Outline each blood parasite and name the species.
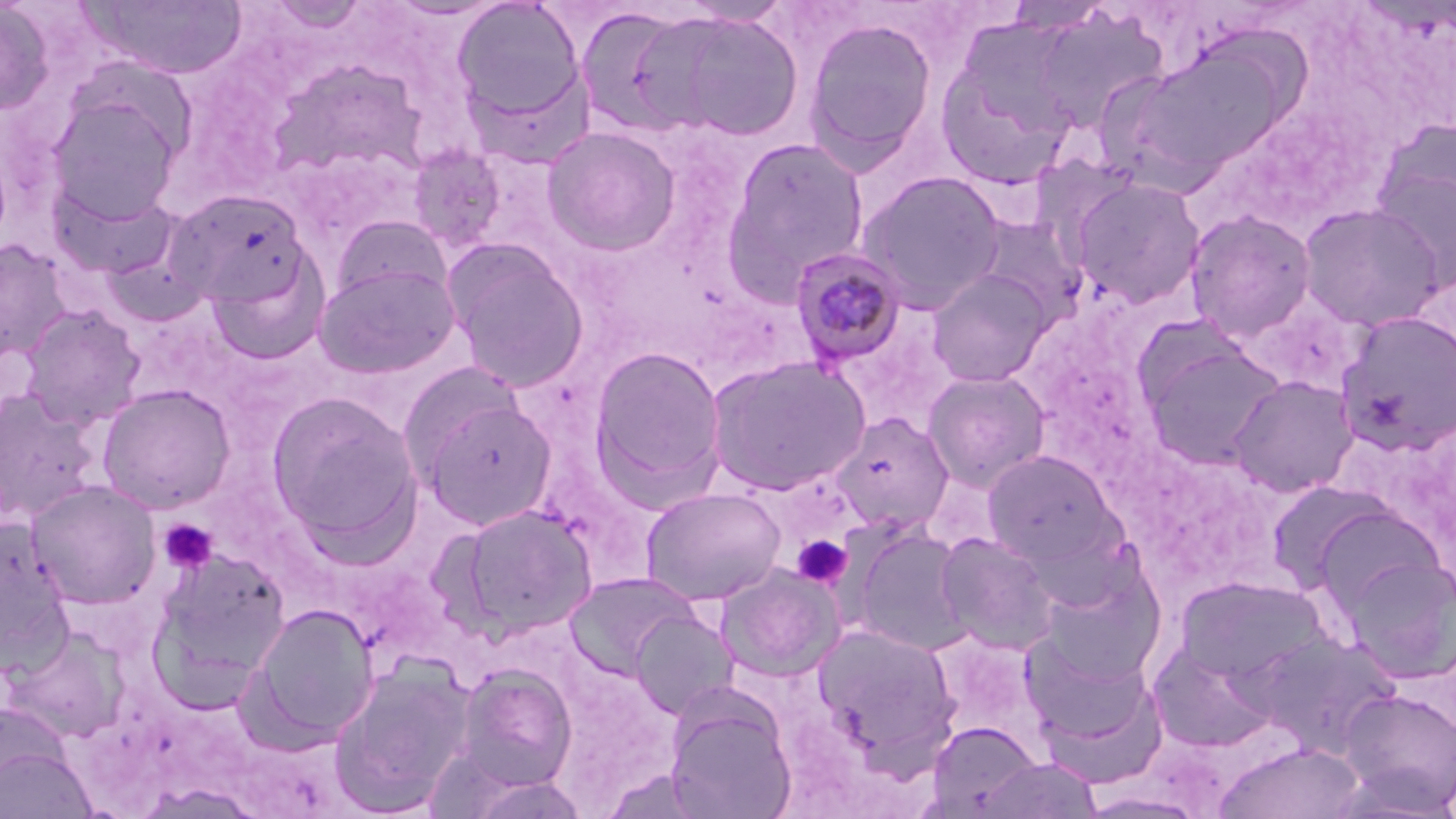

Approximate bounding boxes as named x1/y1/x2/y2 corners in pixels.
Plasmodium malariae-infected red blood cells: (x1=789, y1=247, x2=908, y2=368).
No Plasmodium falciparum, Plasmodium ovale, Plasmodium vivax, Babesia divergens, or Trypanosoma brucei observed.

slide-level diagnosis = Plasmodium malariae
modality = light microscopy
preparation = thin blood smear
magnification = 1000x
platelet locations = approximate bounding boxes as named x1/y1/x2/y2 corners in pixels: (x1=159, y1=519, x2=218, y2=574), (x1=791, y1=535, x2=852, y2=588)
uninfected red blood cell locations = approximate bounding boxes as named x1/y1/x2/y2 corners in pixels: (x1=450, y1=0, x2=588, y2=138), (x1=0, y1=1, x2=54, y2=116), (x1=79, y1=1, x2=250, y2=80), (x1=665, y1=11, x2=806, y2=141), (x1=801, y1=15, x2=939, y2=169), (x1=934, y1=36, x2=1082, y2=192), (x1=1123, y1=40, x2=1296, y2=184), (x1=47, y1=90, x2=185, y2=224), (x1=541, y1=125, x2=682, y2=256), (x1=722, y1=136, x2=871, y2=296), (x1=406, y1=143, x2=508, y2=255), (x1=1370, y1=153, x2=1456, y2=297), (x1=855, y1=170, x2=1008, y2=313), (x1=1070, y1=176, x2=1207, y2=308), (x1=49, y1=177, x2=183, y2=282), (x1=168, y1=188, x2=312, y2=310), (x1=1297, y1=202, x2=1446, y2=332), (x1=1184, y1=209, x2=1317, y2=342), (x1=330, y1=214, x2=453, y2=307), (x1=969, y1=214, x2=1088, y2=325), (x1=0, y1=239, x2=74, y2=363), (x1=442, y1=239, x2=591, y2=393), (x1=205, y1=247, x2=332, y2=364), (x1=314, y1=261, x2=461, y2=379), (x1=927, y1=269, x2=1053, y2=386), (x1=18, y1=305, x2=146, y2=429), (x1=1336, y1=310, x2=1456, y2=455), (x1=1140, y1=337, x2=1286, y2=469), (x1=588, y1=346, x2=729, y2=505), (x1=705, y1=354, x2=871, y2=496), (x1=921, y1=369, x2=1051, y2=492), (x1=1228, y1=375, x2=1358, y2=498), (x1=97, y1=383, x2=237, y2=514), (x1=0, y1=387, x2=102, y2=524), (x1=267, y1=391, x2=422, y2=548), (x1=416, y1=392, x2=559, y2=531), (x1=831, y1=413, x2=954, y2=534), (x1=981, y1=450, x2=1122, y2=571), (x1=26, y1=479, x2=162, y2=609), (x1=1265, y1=482, x2=1397, y2=596), (x1=641, y1=486, x2=786, y2=606), (x1=458, y1=503, x2=598, y2=636), (x1=1308, y1=503, x2=1446, y2=618), (x1=0, y1=520, x2=74, y2=669), (x1=852, y1=528, x2=974, y2=656), (x1=936, y1=532, x2=1061, y2=655), (x1=151, y1=547, x2=291, y2=698), (x1=1341, y1=556, x2=1456, y2=682), (x1=716, y1=564, x2=844, y2=681), (x1=565, y1=571, x2=700, y2=678), (x1=1039, y1=571, x2=1166, y2=686), (x1=1174, y1=576, x2=1329, y2=691), (x1=248, y1=603, x2=378, y2=744), (x1=629, y1=610, x2=738, y2=720), (x1=812, y1=622, x2=961, y2=764), (x1=4, y1=628, x2=129, y2=744), (x1=1252, y1=630, x2=1402, y2=758), (x1=1021, y1=636, x2=1162, y2=758), (x1=1148, y1=644, x2=1280, y2=754), (x1=328, y1=659, x2=475, y2=817), (x1=452, y1=662, x2=579, y2=795), (x1=1337, y1=687, x2=1456, y2=816), (x1=665, y1=696, x2=797, y2=819), (x1=927, y1=720, x2=1043, y2=815), (x1=0, y1=735, x2=97, y2=819), (x1=1215, y1=742, x2=1364, y2=819), (x1=979, y1=756, x2=1102, y2=818), (x1=1077, y1=791, x2=1208, y2=818)
stain = May-Grünwald-Giemsa
field of view = one of a larger specimen
image size = 1456×819 pixels